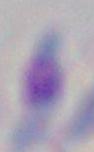
{
  "magnification": "1000x",
  "modality": "micrograph",
  "identification": "Toxoplasma gondii"
}